Report the malaria status of this cell.
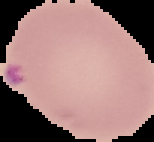

It is parasitized.

image size = 154×142 pixels
image type = segmented cell region on a black background
preparation = thin blood film